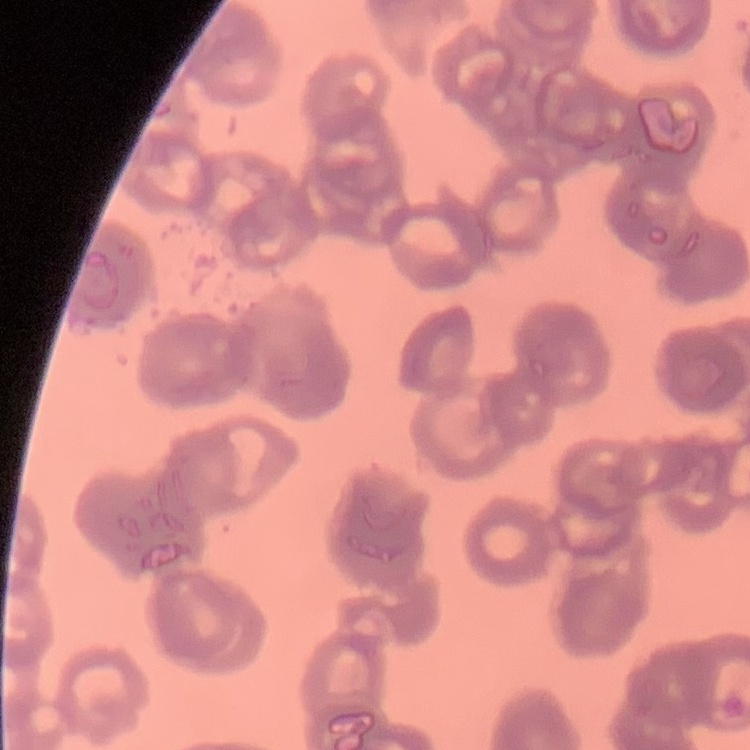

red blood cell morphology = rouleaux formation
preparation = thin blood smear
image type = square crop of a larger photomicrograph
stain = Field's or Giemsa